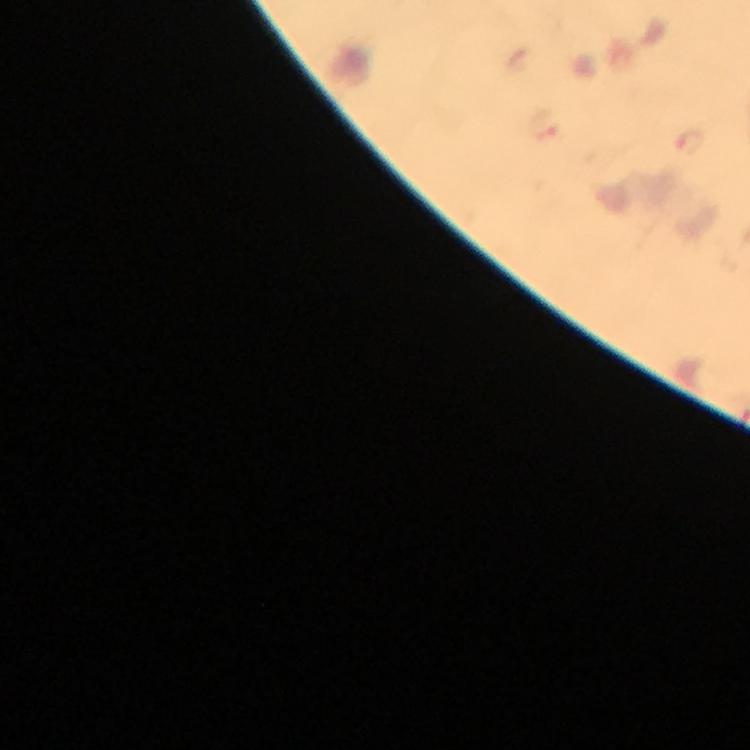
Approximate centers as {x, y} in pixels. Malaria parasite locations: {544, 124}, {691, 143}. Giemsa-stained preparation. Immersion oil was used. A crop from one field of view. Photographed with a smartphone mounted on the microscope. From a malaria diagnostic workup. Thick blood film. At 100x magnification. Image is 750×750 pixels.